Assess this cell for malaria.
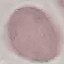

Uninfected.

{
  "preparation": "thin blood smear",
  "capture": "smartphone camera at the microscope eyepiece",
  "stain": "Giemsa",
  "image_type": "automatically extracted cell patch, resized to 64 × 64 pixels"
}